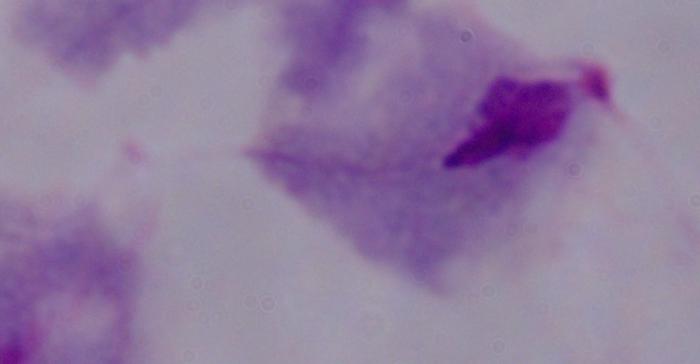
{
  "modality": "micrograph",
  "identification": "trichomonad",
  "magnification": "1000x"
}